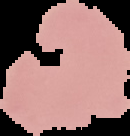
Segmented cell region on a black background. From a thin blood film. Malaria status: uninfected. Image is 130×136 pixels.